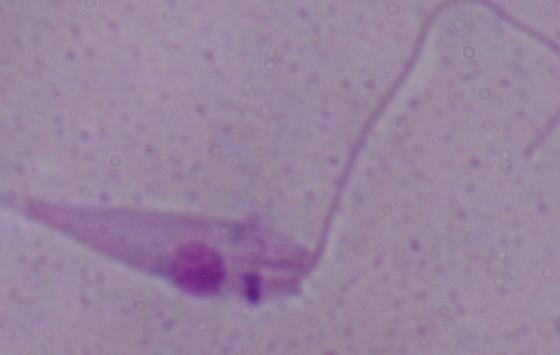
Captured at 1000x magnification. A Leishmania parasite is shown. Micrograph.